Locate and identify every blood parasite.
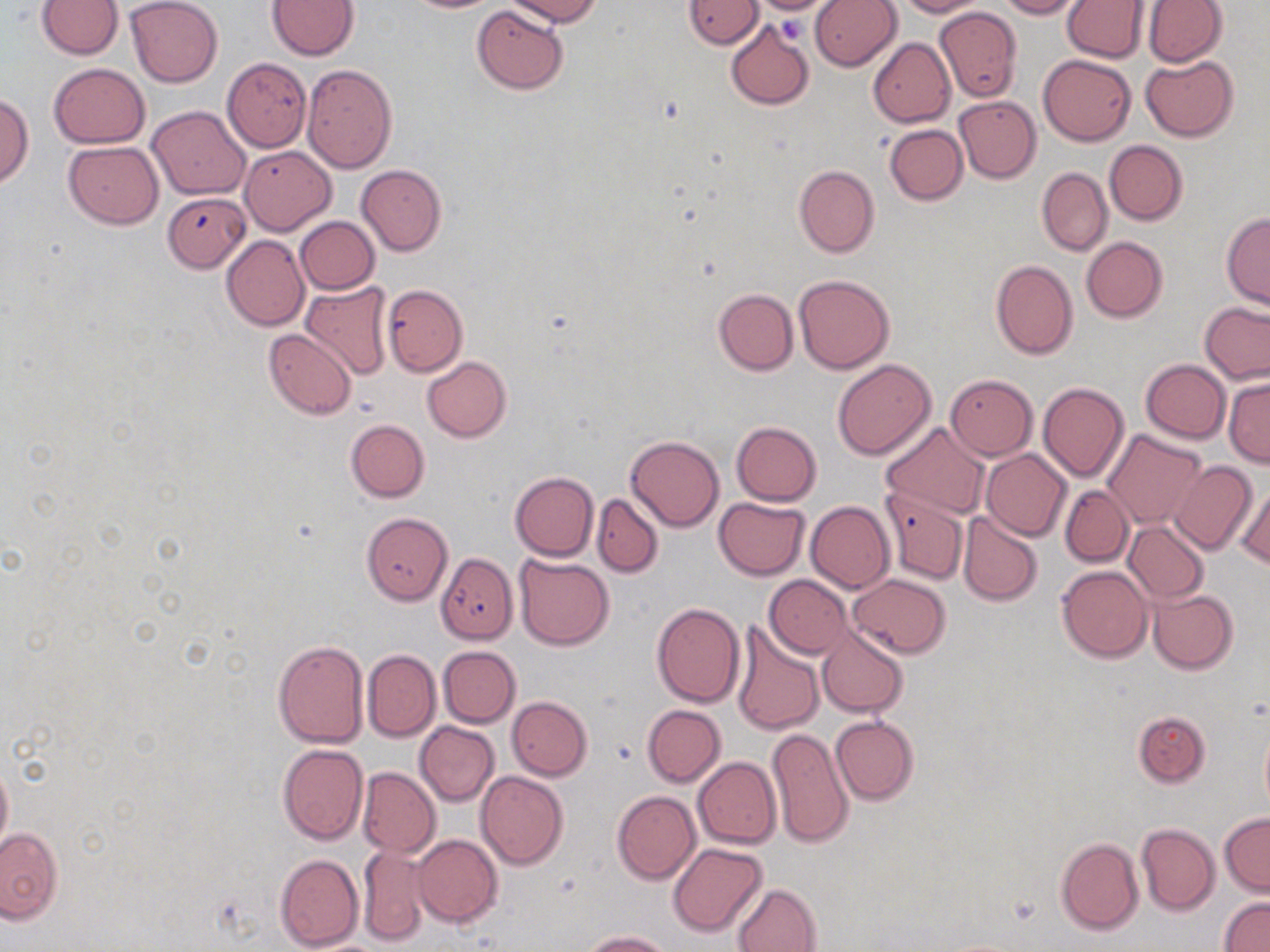
No blood parasites seen.

Summary:
  - Coordinate format: approximate bounding boxes as named x1/y1/x2/y2 corners in pixels
  - Uninfected red blood cell locations: (x1=37, y1=0, x2=123, y2=59), (x1=126, y1=0, x2=222, y2=87), (x1=403, y1=0, x2=501, y2=13), (x1=504, y1=0, x2=601, y2=26), (x1=751, y1=0, x2=835, y2=15), (x1=895, y1=0, x2=988, y2=17), (x1=996, y1=0, x2=1083, y2=19), (x1=1142, y1=0, x2=1227, y2=67), (x1=267, y1=1, x2=358, y2=59), (x1=684, y1=1, x2=763, y2=48), (x1=809, y1=1, x2=901, y2=71), (x1=1061, y1=1, x2=1148, y2=62), (x1=471, y1=5, x2=568, y2=94), (x1=933, y1=7, x2=1022, y2=102), (x1=725, y1=20, x2=814, y2=111), (x1=871, y1=21, x2=1023, y2=119), (x1=868, y1=38, x2=955, y2=127), (x1=1037, y1=53, x2=1137, y2=146), (x1=1141, y1=56, x2=1238, y2=141), (x1=223, y1=57, x2=311, y2=152), (x1=302, y1=62, x2=398, y2=174), (x1=48, y1=63, x2=150, y2=148), (x1=0, y1=94, x2=33, y2=187), (x1=953, y1=96, x2=1041, y2=183), (x1=147, y1=106, x2=251, y2=199), (x1=883, y1=124, x2=967, y2=205), (x1=1105, y1=140, x2=1188, y2=225), (x1=63, y1=141, x2=164, y2=228), (x1=239, y1=146, x2=336, y2=236), (x1=356, y1=164, x2=446, y2=256), (x1=794, y1=164, x2=879, y2=257), (x1=1037, y1=169, x2=1112, y2=255), (x1=167, y1=193, x2=256, y2=274), (x1=1221, y1=212, x2=1269, y2=308), (x1=294, y1=217, x2=379, y2=294), (x1=221, y1=236, x2=310, y2=330), (x1=1081, y1=237, x2=1167, y2=323), (x1=990, y1=260, x2=1079, y2=360), (x1=793, y1=274, x2=896, y2=374), (x1=301, y1=281, x2=393, y2=379), (x1=382, y1=285, x2=468, y2=375), (x1=713, y1=288, x2=798, y2=375), (x1=1199, y1=301, x2=1269, y2=384), (x1=263, y1=328, x2=357, y2=419), (x1=422, y1=356, x2=511, y2=442), (x1=832, y1=358, x2=936, y2=460), (x1=1140, y1=359, x2=1231, y2=443), (x1=945, y1=374, x2=1038, y2=460), (x1=1224, y1=375, x2=1270, y2=467), (x1=1038, y1=383, x2=1129, y2=482), (x1=345, y1=419, x2=429, y2=502), (x1=881, y1=421, x2=989, y2=519), (x1=732, y1=422, x2=821, y2=506), (x1=1101, y1=429, x2=1207, y2=529), (x1=625, y1=433, x2=725, y2=532), (x1=981, y1=449, x2=1071, y2=541), (x1=1168, y1=461, x2=1257, y2=555), (x1=509, y1=471, x2=598, y2=561), (x1=1234, y1=481, x2=1270, y2=570), (x1=1060, y1=486, x2=1133, y2=566), (x1=881, y1=489, x2=968, y2=584), (x1=591, y1=494, x2=663, y2=577), (x1=713, y1=496, x2=810, y2=579), (x1=805, y1=501, x2=895, y2=592), (x1=361, y1=512, x2=454, y2=605), (x1=956, y1=512, x2=1043, y2=607), (x1=1123, y1=521, x2=1209, y2=603), (x1=437, y1=553, x2=518, y2=643), (x1=514, y1=554, x2=614, y2=650), (x1=1057, y1=565, x2=1153, y2=662), (x1=847, y1=574, x2=952, y2=656), (x1=765, y1=575, x2=851, y2=658), (x1=1147, y1=589, x2=1239, y2=675), (x1=652, y1=602, x2=745, y2=707), (x1=729, y1=617, x2=826, y2=734), (x1=817, y1=626, x2=908, y2=718), (x1=273, y1=639, x2=370, y2=748), (x1=439, y1=646, x2=521, y2=727), (x1=363, y1=649, x2=441, y2=742), (x1=506, y1=696, x2=592, y2=780), (x1=643, y1=705, x2=725, y2=786), (x1=1133, y1=710, x2=1210, y2=787), (x1=830, y1=716, x2=919, y2=805), (x1=1259, y1=718, x2=1270, y2=820), (x1=415, y1=722, x2=499, y2=806), (x1=767, y1=728, x2=853, y2=849), (x1=277, y1=744, x2=369, y2=846), (x1=0, y1=755, x2=12, y2=860), (x1=693, y1=757, x2=780, y2=849), (x1=358, y1=767, x2=440, y2=857), (x1=476, y1=771, x2=568, y2=869), (x1=611, y1=790, x2=700, y2=884), (x1=1220, y1=813, x2=1270, y2=895), (x1=1136, y1=823, x2=1219, y2=915), (x1=0, y1=826, x2=63, y2=923), (x1=413, y1=834, x2=502, y2=928), (x1=1055, y1=837, x2=1143, y2=935), (x1=357, y1=843, x2=432, y2=946), (x1=667, y1=843, x2=769, y2=936), (x1=275, y1=853, x2=364, y2=951), (x1=731, y1=882, x2=823, y2=952), (x1=1219, y1=895, x2=1270, y2=952), (x1=579, y1=929, x2=673, y2=951)
  - Platelet locations: (x1=778, y1=14, x2=807, y2=45)
  - Slide-level diagnosis: negative for blood parasites
  - Image size: 1270×952 pixels
  - Modality: optical microscopy
  - Field of view: one of a larger specimen
  - Magnification: 1000x
  - Stain: May-Grünwald-Giemsa
  - Preparation: thin blood film